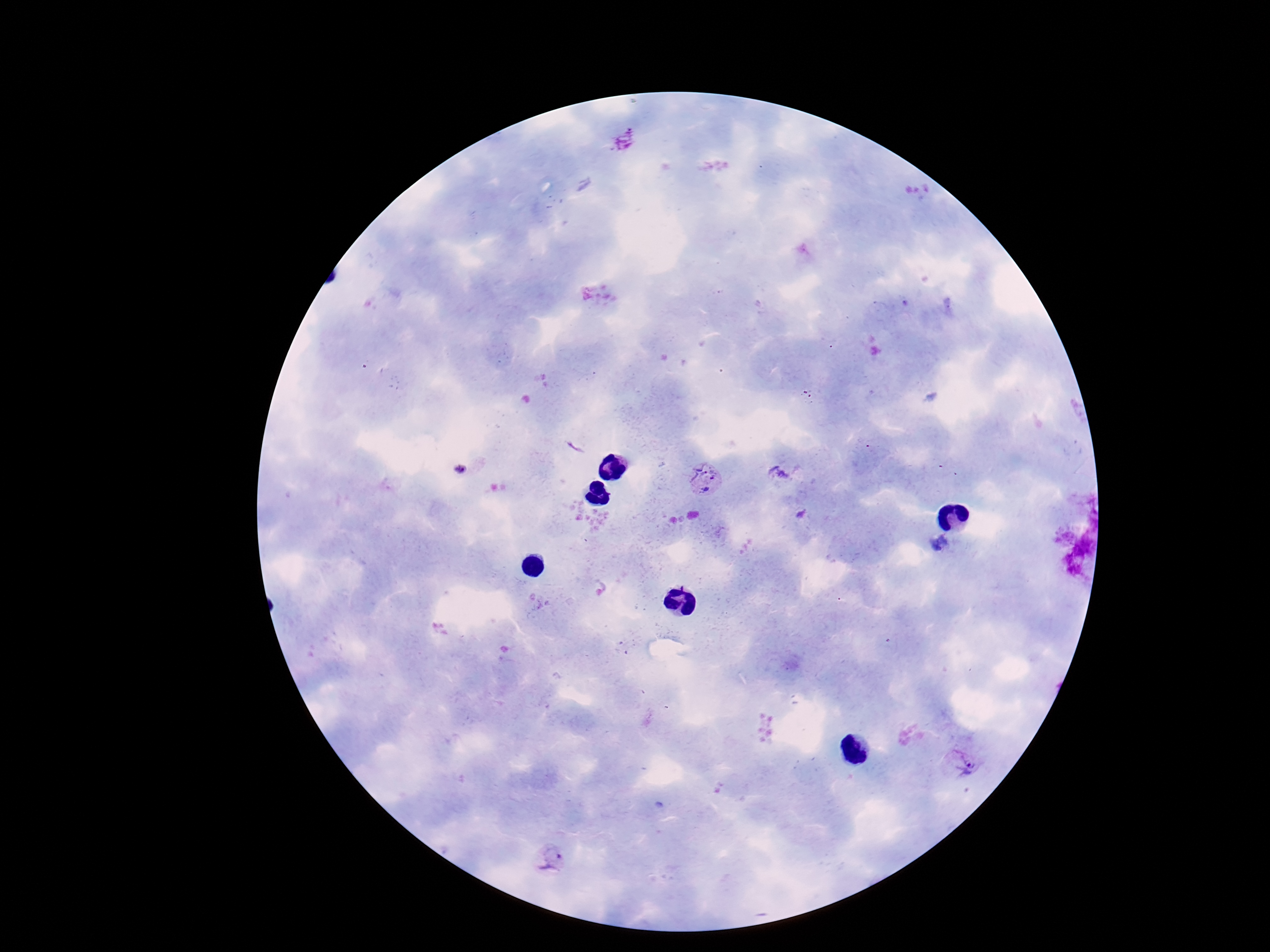

Approximate object centers, in pixels from the top-left corner. Plasmodium parasite locations: (x=625, y=141), (x=783, y=475), (x=707, y=478), (x=962, y=766), (x=550, y=859). Single field of view. Thick peripheral-blood smear. Photographed through the microscope eyepiece with a smartphone camera. Giemsa stain. 100x magnification. Patient malaria status: positive. Image is 1270×952 pixels.